Name the parasite shown.
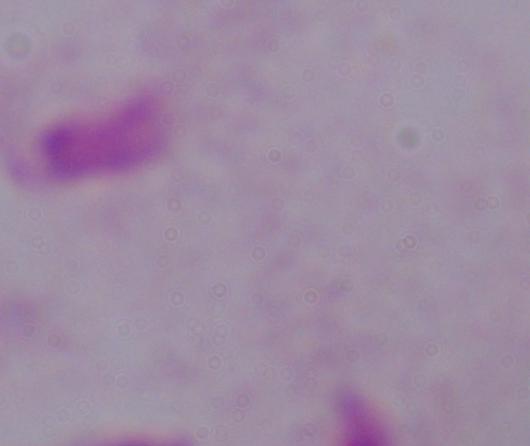
This is a trichomonad.

modality: photomicrograph
magnification: 1000x